Locate every Plasmodium ovale-infected red blood cell.
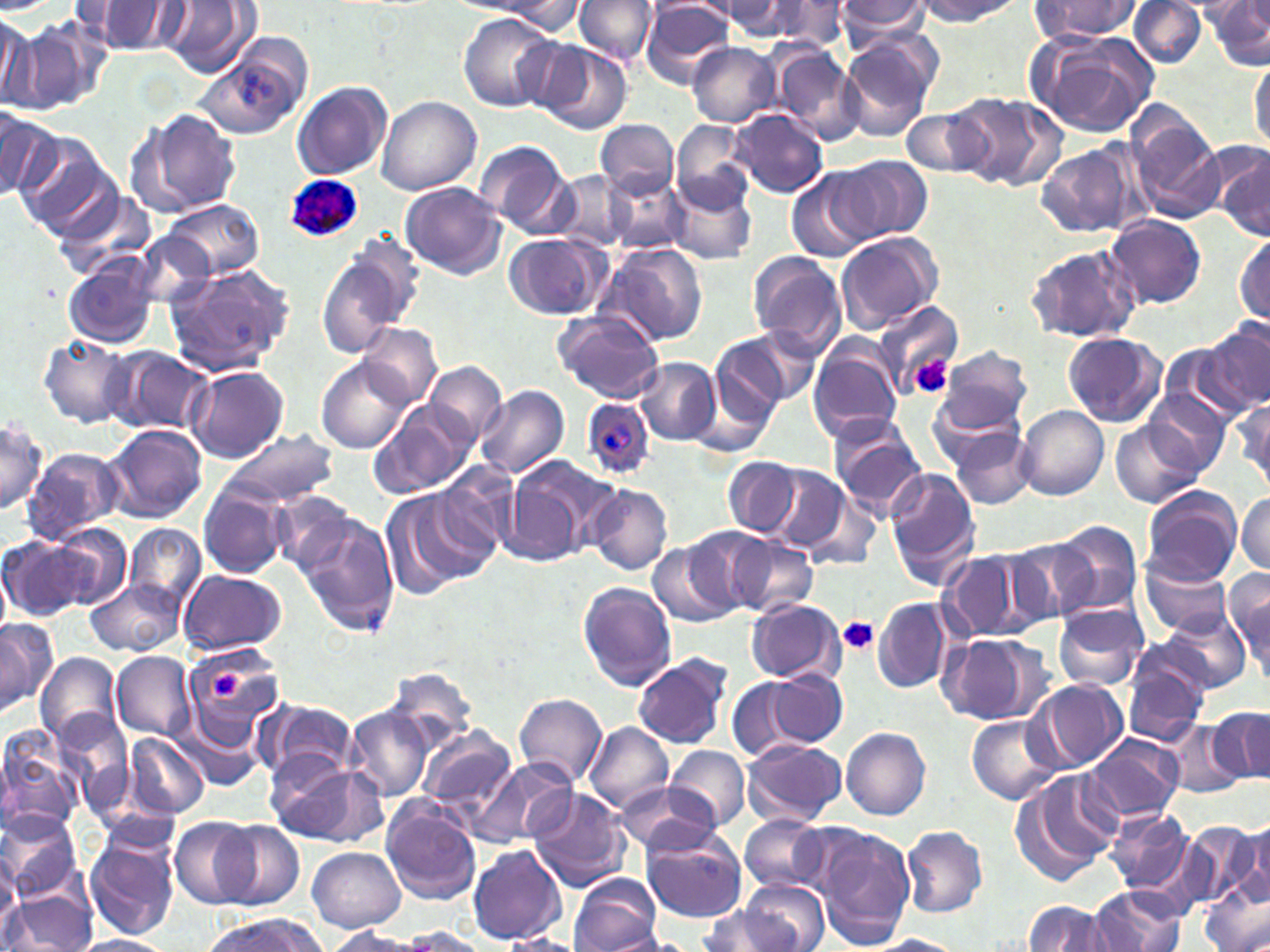
Approximate bounding boxes as (x1,y1)-(x2,y2) corner pairs in pixels.
Plasmodium ovale-infected red blood cells: (288,175)-(365,243), (579,397)-(655,479).

slide_level_diagnosis: Plasmodium ovale
image_size: 1270×952 pixels
modality: optical microscopy
preparation: thin blood film
uninfected_red_blood_cell_locations: 'approximate bounding boxes as (x1,y1)-(x2,y2) corner pairs in pixels: (573,0)-(657,65), (838,0)-(933,44), (912,0)-(1022,26), (1207,0)-(1270,69), (482,1)-(584,33), (715,1)-(806,37), (1028,1)-(1143,41), (1129,1)-(1208,68), (161,2)-(256,78), (639,2)-(735,87), (769,2)-(851,52), (84,3)-(186,56), (458,13)-(556,112), (0,15)-(36,109), (10,23)-(94,113), (1027,29)-(1159,138), (838,35)-(937,138), (689,41)-(781,128), (536,43)-(632,134), (193,44)-(307,141), (771,44)-(862,143), (1249,56)-(1270,151), (292,81)-(393,180), (949,91)-(1062,191), (377,96)-(481,195), (1126,103)-(1225,225), (901,106)-(992,178), (126,107)-(244,219), (0,109)-(56,198), (729,109)-(829,198), (597,119)-(677,198), (672,120)-(752,214), (13,133)-(115,237), (474,140)-(573,237), (1035,140)-(1144,241), (1213,147)-(1270,240), (834,156)-(932,243), (549,170)-(632,249), (602,172)-(690,254), (786,172)-(873,262), (667,179)-(756,265), (401,184)-(505,278), (54,189)-(155,281), (166,198)-(262,279), (1104,215)-(1207,310), (835,231)-(943,332), (133,233)-(219,310), (503,233)-(606,318), (1234,233)-(1269,324), (1024,242)-(1142,345), (600,244)-(709,349), (315,246)-(420,360), (747,251)-(850,360), (64,261)-(158,349), (163,263)-(294,376), (872,300)-(962,393), (553,311)-(664,403), (1202,320)-(1270,415), (360,323)-(442,407), (743,327)-(822,406), (1061,332)-(1168,427), (711,334)-(793,423), (39,335)-(137,428), (106,346)-(212,437), (808,346)-(903,445), (935,347)-(1032,434), (635,356)-(720,446), (318,358)-(414,454), (425,361)-(506,446), (188,367)-(289,462), (475,384)-(568,481), (1141,389)-(1233,479), (1234,396)-(1269,492), (371,402)-(480,502), (1016,404)-(1108,500), (828,416)-(927,517), (1,417)-(48,514), (1112,418)-(1205,510), (103,423)-(207,524), (946,424)-(1036,510), (221,428)-(337,508), (21,447)-(124,545), (507,453)-(620,559), (722,458)-(799,537), (439,462)-(522,557), (759,465)-(852,554), (884,468)-(981,586), (586,484)-(672,575), (198,485)-(290,579), (1141,485)-(1243,587), (269,487)-(358,573), (379,487)-(483,601), (1235,492)-(1269,574), (800,496)-(883,570), (294,509)-(399,638), (1052,521)-(1142,616), (126,522)-(206,610), (47,524)-(130,610), (682,527)-(774,615), (722,534)-(820,617), (0,535)-(85,622), (1006,535)-(1101,626), (647,540)-(741,627), (938,549)-(1048,644), (1139,557)-(1234,639), (1224,569)-(1270,676), (178,570)-(288,658), (87,578)-(184,656), (578,581)-(677,691), (870,596)-(955,694), (744,598)-(845,685), (1053,603)-(1148,691), (1152,611)-(1246,694), (0,618)-(57,714), (938,632)-(1052,727), (179,641)-(287,749), (36,651)-(121,745), (111,651)-(195,740), (632,654)-(733,750), (1121,661)-(1207,748), (383,667)-(478,755), (768,670)-(847,746), (728,678)-(806,764), (1032,678)-(1129,771), (515,693)-(608,787), (259,698)-(360,783), (51,706)-(131,812), (1207,706)-(1269,786), (347,707)-(433,803), (173,708)-(264,795), (964,715)-(1064,805), (1164,721)-(1245,798), (585,722)-(674,814), (418,725)-(517,815), (842,726)-(931,819), (0,732)-(81,837), (124,732)-(210,819), (1083,733)-(1184,824), (742,739)-(847,827), (664,745)-(751,831), (473,758)-(576,849), (268,761)-(383,845), (1011,769)-(1119,885), (618,784)-(716,856), (529,788)-(635,892), (380,796)-(483,905), (0,807)-(84,900), (1103,809)-(1196,898), (740,816)-(829,893), (170,817)-(261,909), (1233,819)-(1269,906), (214,821)-(306,911), (1186,821)-(1266,912), (901,826)-(987,918), (806,827)-(911,949), (84,830)-(180,941), (642,830)-(747,923), (467,843)-(566,946), (308,846)-(406,932), (0,859)-(24,937), (568,873)-(662,952), (740,878)-(827,952), (1203,882)-(1269,952), (1089,887)-(1186,951), (5,890)-(94,950), (1021,900)-(1115,952), (696,905)-(790,952), (198,914)-(327,951), (325,927)-(428,952), (396,928)-(488,950), (597,932)-(693,952), (67,934)-(177,952), (498,934)-(591,952), (865,935)-(966,952)'
field_of_view: single
platelet_locations: 'approximate bounding boxes as (x1,y1)-(x2,y2) corner pairs in pixels: (909,353)-(953,400), (837,618)-(881,658), (206,669)-(247,702)'
magnification: 1000x
stain: May-Grünwald-Giemsa